Comment on the morphology of the red blood cells.
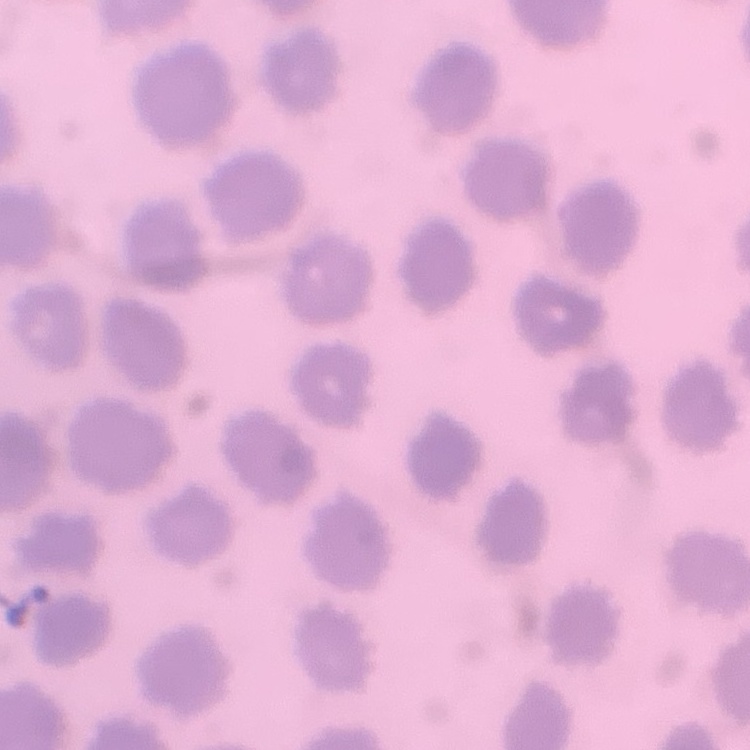
They show no rouleaux formation.

Stained with either Field's or Giemsa. Thin blood film. One tile cut from a larger photomicrograph.